Locate every Plasmodium falciparum-infected red blood cell.
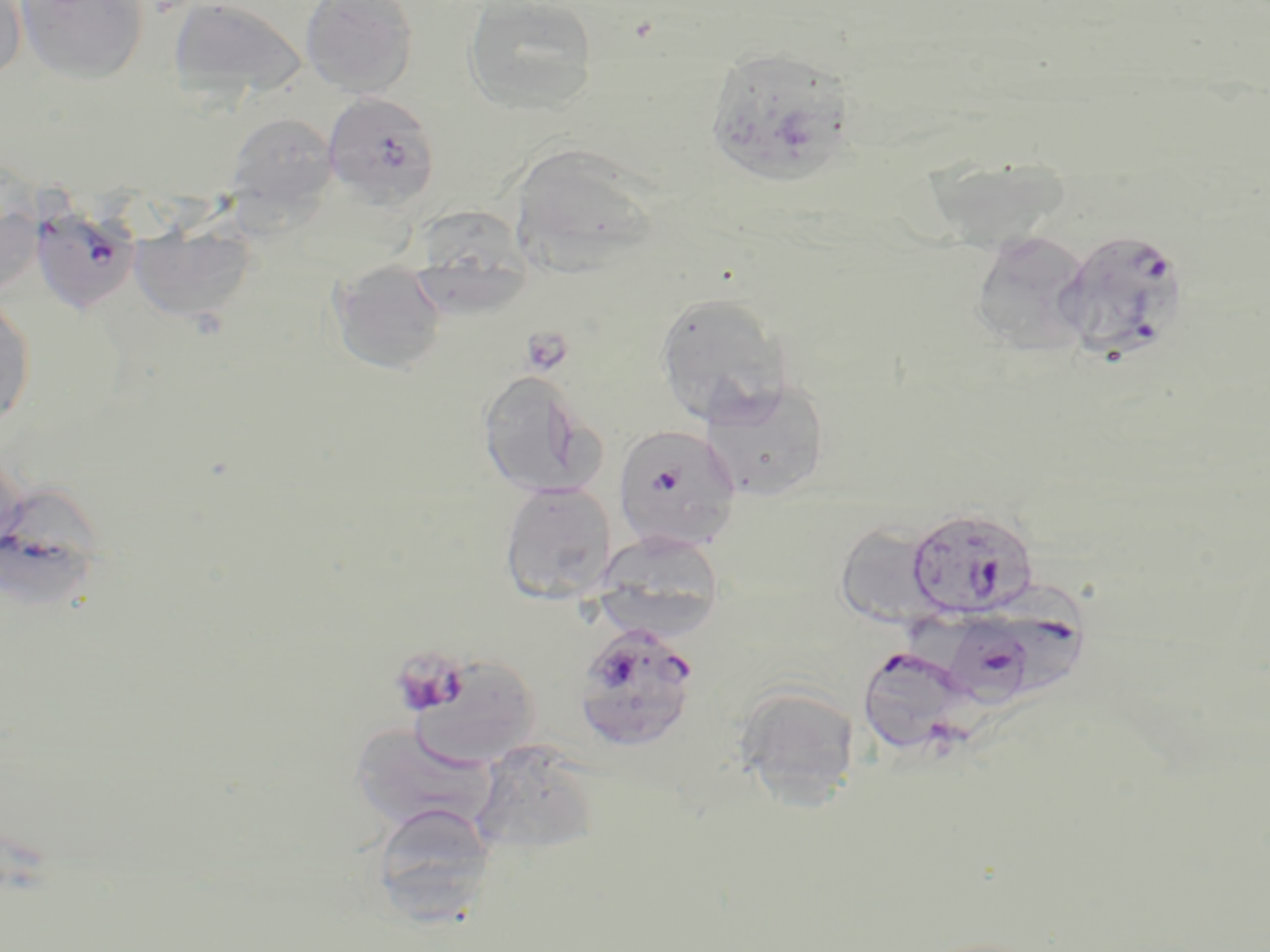
Approximate bounding boxes as (x1,y1)-(x2,y2) corner pairs in pixels.
Plasmodium falciparum-infected red blood cells: (707,53)-(855,182), (322,91)-(441,210), (30,202)-(141,314), (1056,228)-(1190,363), (612,424)-(741,552), (906,506)-(1038,620), (1002,583)-(1092,699), (944,617)-(1035,712), (573,622)-(702,753), (863,644)-(983,752).

Platelet locations: (399,653)-(466,713). Uninfected red blood cell locations: (0,0)-(28,82), (15,0)-(148,84), (169,0)-(306,102), (300,0)-(419,98), (463,0)-(598,116), (224,112)-(338,219), (510,147)-(661,278), (923,155)-(1072,251), (0,202)-(44,299), (410,204)-(531,313), (129,220)-(255,325), (969,230)-(1094,358), (329,259)-(448,376), (653,291)-(792,427), (0,295)-(36,429), (477,370)-(603,499), (700,378)-(830,502), (499,482)-(617,604), (0,488)-(107,608), (834,523)-(946,629), (593,532)-(726,639), (401,652)-(543,768), (736,685)-(860,807), (349,722)-(502,838), (470,741)-(600,856), (369,801)-(498,923). Slide-level diagnosis: Plasmodium falciparum. One field of a larger specimen. Image is 1270×952 pixels. Light microscopy. Thin blood film. May-Grünwald-Giemsa-stained preparation. 1000x magnification.